State which parasite is depicted.
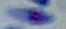

This is Toxoplasma gondii.

Captured at 1000x magnification. Micrograph.